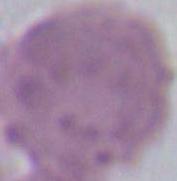
Summary:
  - Magnification: 1000x
  - Modality: micrograph
  - Identification: erythrocyte